Classify this cell by malaria status.
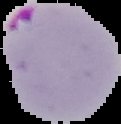
Parasitized.

image size = 121×124 pixels
image type = cell region segmented out of the field of view; surrounding area masked to black
preparation = thin blood smear